Name the parasite shown.
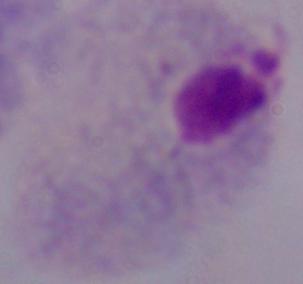
This is a trichomonad.

Photomicrograph. 1000x magnification.